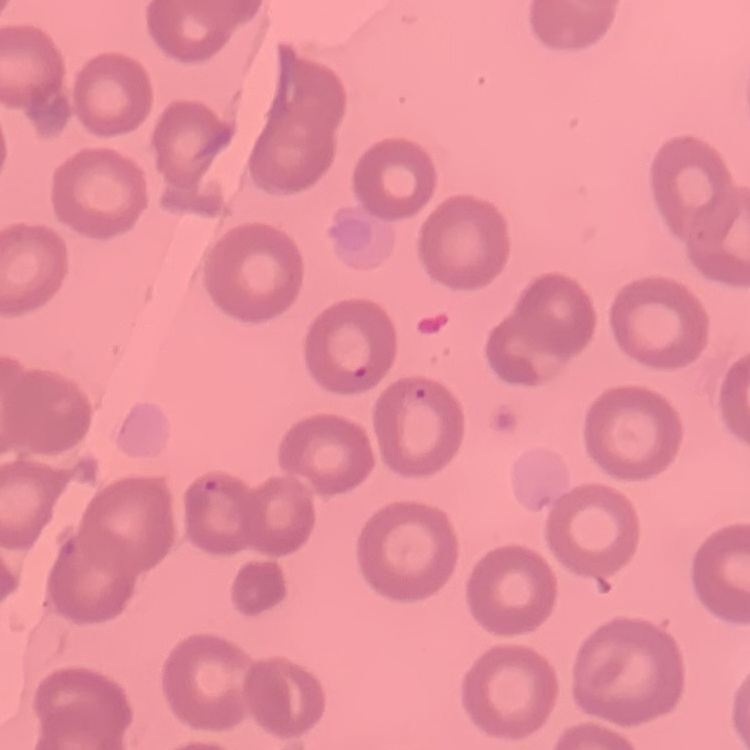
Summary:
  - Erythrocyte morphology: no rouleaux formation
  - Stain: Field's or Giemsa
  - Image type: square crop of a larger photomicrograph
  - Preparation: thin blood film